Give the preparation type.
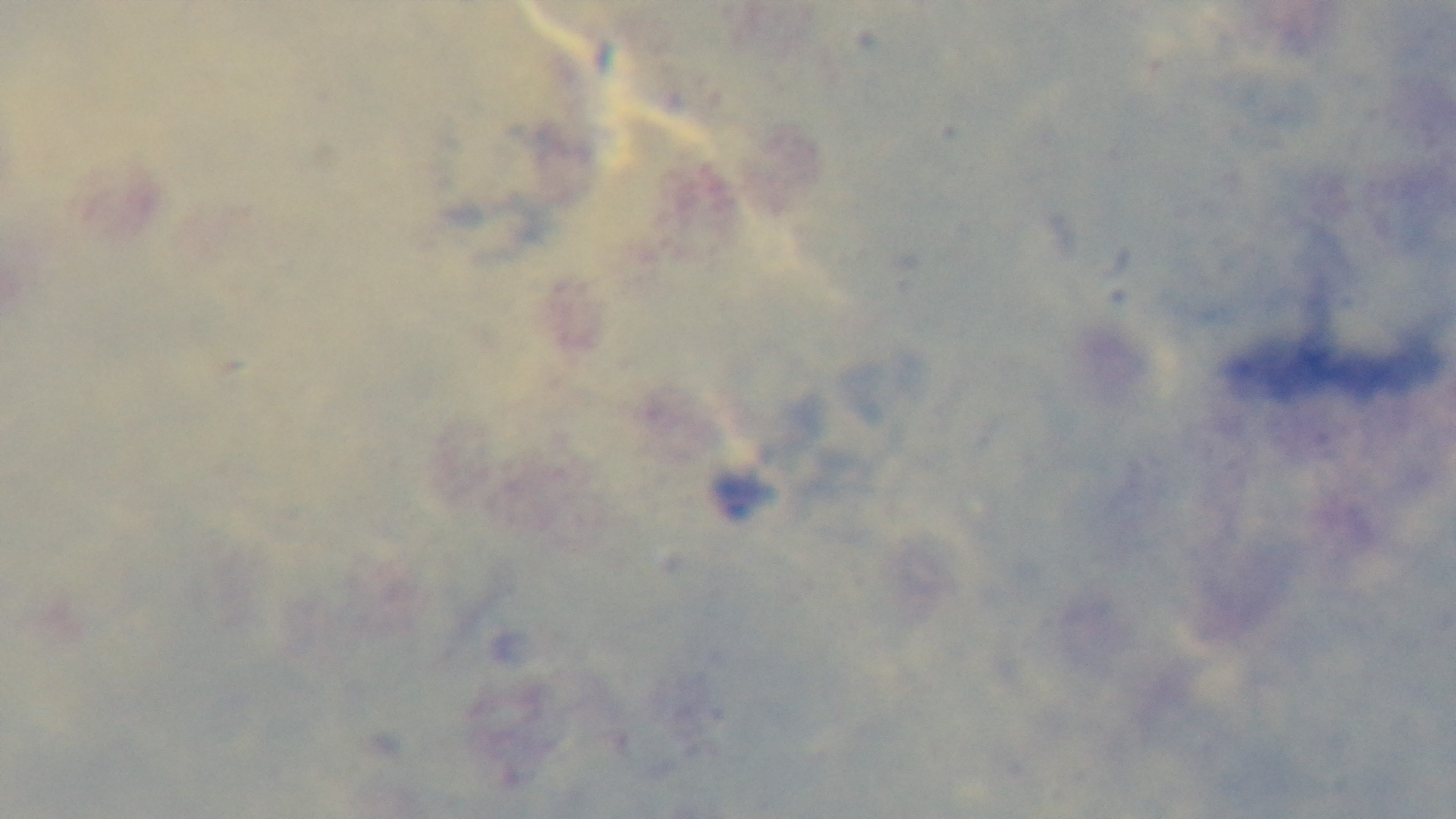
Thick.

modality: light microscopy
objective: 100x oil immersion
capture: mounted 4K digital camera
stain: Giemsa
field_of_view: one from the slide
malaria_status: uninfected